Report the malaria status.
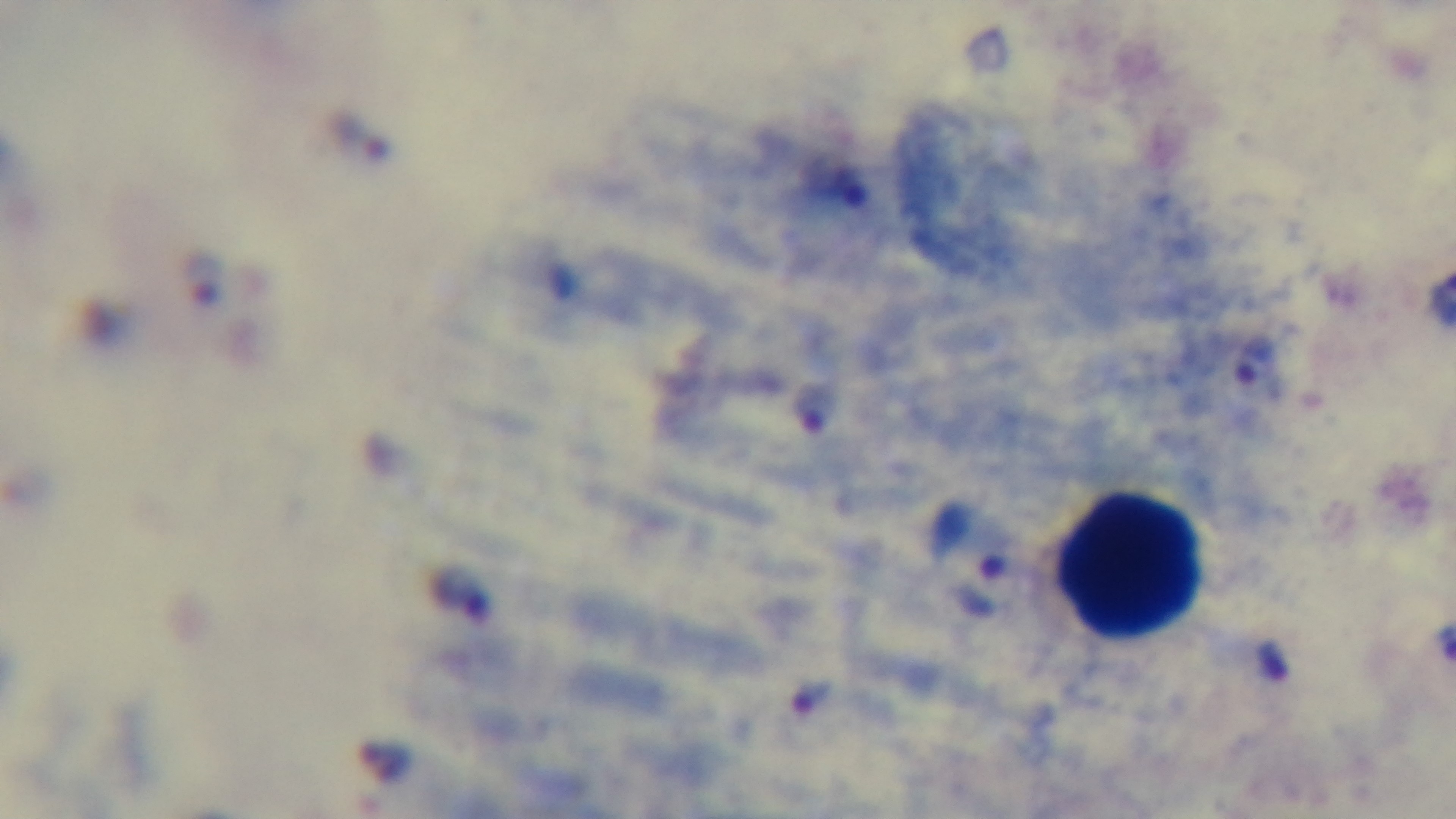

Positive.

Summary:
  - Preparation: thick
  - Field of view: one from the slide
  - Stain: Giemsa
  - Capture: mounted 4K digital camera
  - Objective: 100x oil immersion
  - Modality: light microscopy